Assess this cell for malaria.
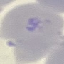
Uninfected.

Giemsa stain. Thin blood smear. Photographed with a smartphone camera at the microscope eyepiece. Automatically extracted cell patch, resized to 64 × 64 pixels.